Locate leukocytes (white blood cells).
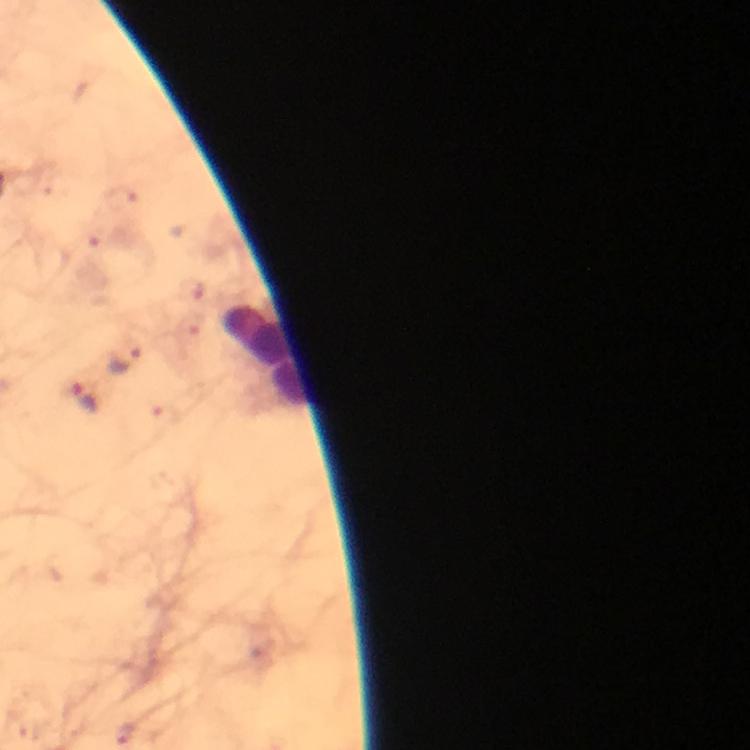

Approximate centers as {x, y} in pixels.
Leukocytes: {264, 358}.

stain = Giemsa
malaria parasite locations = approximate centers as {x, y} in pixels: {126, 359}, {85, 398}
capture = smartphone camera through the microscope
context = from a malaria diagnostic workup
magnification = 100x
image size = 750×750 pixels
immersion oil = applied
preparation = thick blood film
cropped from = one field of view